Comment on the morphology of the red blood cells.
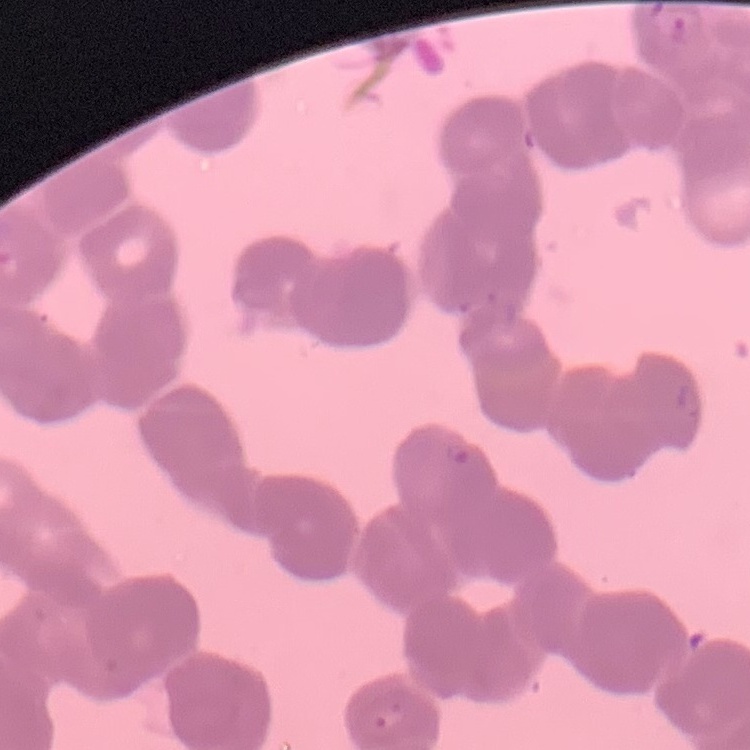

Rouleaux formation.

Summary:
  - Image type: square crop of a larger photomicrograph
  - Stain: Field's or Giemsa
  - Preparation: thin blood smear